Name the parasite shown.
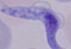

This is a trypanosome.

Captured at 1000x magnification. Photomicrograph.